Give the extent of all Plasmodium malariae-infected red blood cells.
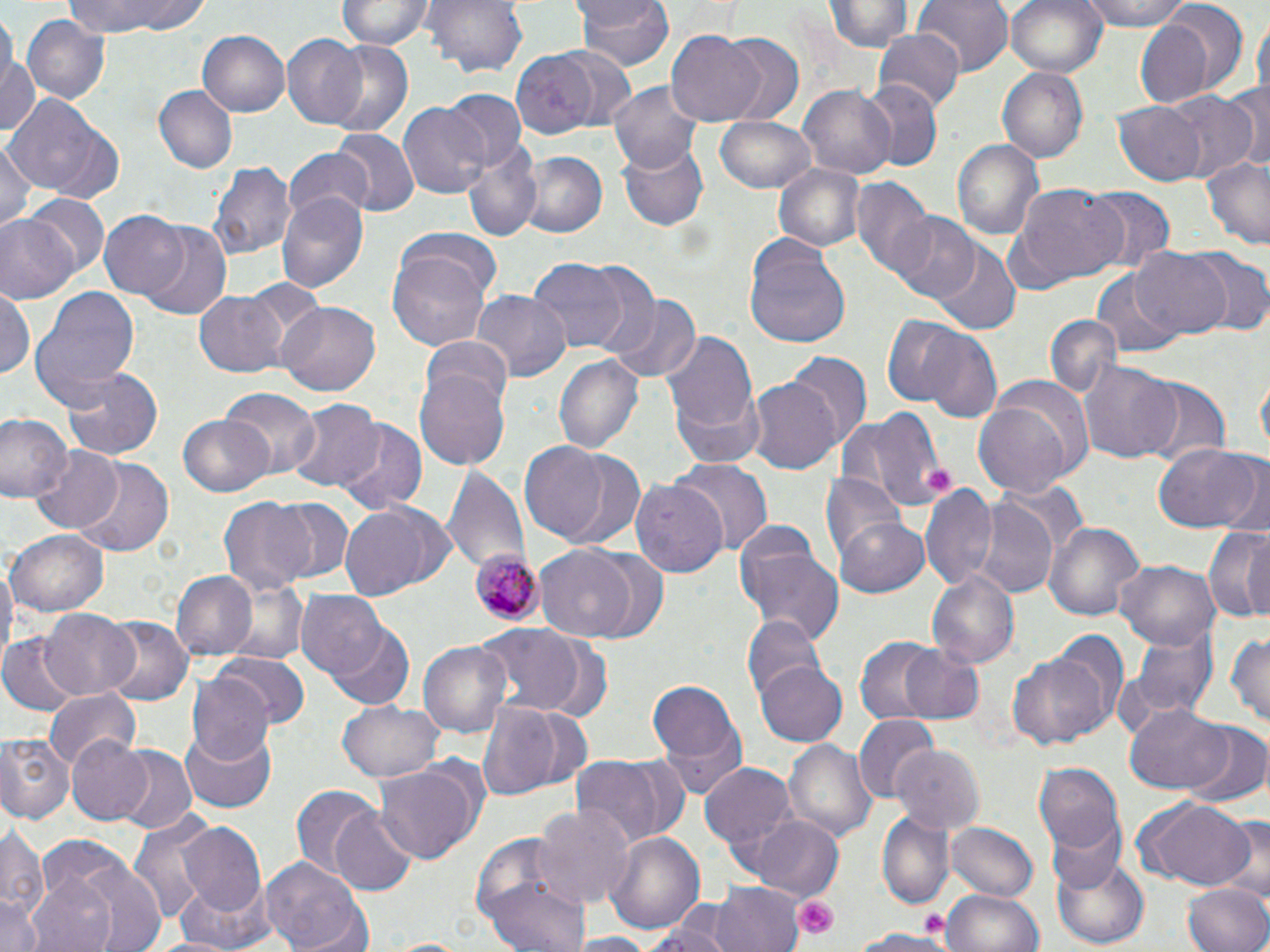

Approximate bounding boxes as named x1/y1/x2/y2 corners in pixels.
Plasmodium malariae-infected red blood cells: (x1=472, y1=549, x2=541, y2=626).

Platelet locations: (x1=795, y1=894, x2=840, y2=938), (x1=917, y1=909, x2=950, y2=945). Uninfected red blood cell locations: (x1=62, y1=0, x2=211, y2=38), (x1=424, y1=0, x2=529, y2=78), (x1=574, y1=0, x2=675, y2=74), (x1=826, y1=0, x2=909, y2=53), (x1=914, y1=0, x2=1013, y2=74), (x1=1006, y1=0, x2=1107, y2=80), (x1=1075, y1=0, x2=1200, y2=30), (x1=335, y1=1, x2=434, y2=52), (x1=4, y1=10, x2=19, y2=95), (x1=1134, y1=13, x2=1228, y2=106), (x1=1253, y1=14, x2=1269, y2=102), (x1=23, y1=15, x2=109, y2=103), (x1=197, y1=30, x2=290, y2=118), (x1=874, y1=30, x2=965, y2=114), (x1=719, y1=31, x2=804, y2=121), (x1=665, y1=32, x2=768, y2=122), (x1=280, y1=34, x2=369, y2=128), (x1=322, y1=41, x2=414, y2=138), (x1=0, y1=43, x2=40, y2=144), (x1=548, y1=43, x2=640, y2=133), (x1=509, y1=51, x2=614, y2=139), (x1=997, y1=67, x2=1089, y2=163), (x1=858, y1=79, x2=941, y2=170), (x1=607, y1=80, x2=707, y2=174), (x1=1226, y1=82, x2=1270, y2=171), (x1=155, y1=87, x2=237, y2=173), (x1=799, y1=87, x2=894, y2=178), (x1=441, y1=91, x2=527, y2=171), (x1=4, y1=92, x2=115, y2=199), (x1=1164, y1=92, x2=1259, y2=183), (x1=397, y1=101, x2=489, y2=200), (x1=1112, y1=103, x2=1205, y2=184), (x1=713, y1=115, x2=816, y2=194), (x1=331, y1=128, x2=419, y2=217), (x1=953, y1=138, x2=1045, y2=244), (x1=0, y1=139, x2=38, y2=234), (x1=616, y1=139, x2=707, y2=231), (x1=462, y1=142, x2=541, y2=240), (x1=282, y1=148, x2=374, y2=224), (x1=521, y1=151, x2=607, y2=239), (x1=1201, y1=156, x2=1270, y2=248), (x1=209, y1=160, x2=295, y2=260), (x1=774, y1=163, x2=865, y2=252), (x1=853, y1=180, x2=938, y2=281), (x1=1016, y1=185, x2=1130, y2=286), (x1=1085, y1=189, x2=1175, y2=270), (x1=277, y1=190, x2=369, y2=292), (x1=25, y1=194, x2=110, y2=278), (x1=101, y1=212, x2=192, y2=300), (x1=888, y1=212, x2=981, y2=304), (x1=0, y1=215, x2=77, y2=305), (x1=138, y1=224, x2=230, y2=319), (x1=399, y1=230, x2=502, y2=303), (x1=741, y1=239, x2=852, y2=352), (x1=931, y1=245, x2=1021, y2=333), (x1=1133, y1=247, x2=1233, y2=339), (x1=388, y1=250, x2=489, y2=349), (x1=1186, y1=251, x2=1270, y2=337), (x1=528, y1=257, x2=628, y2=355), (x1=581, y1=266, x2=663, y2=359), (x1=1090, y1=268, x2=1184, y2=359), (x1=31, y1=287, x2=141, y2=408), (x1=0, y1=289, x2=35, y2=381), (x1=473, y1=291, x2=569, y2=381), (x1=193, y1=293, x2=288, y2=375), (x1=605, y1=296, x2=699, y2=384), (x1=277, y1=302, x2=380, y2=396), (x1=1043, y1=315, x2=1123, y2=401), (x1=879, y1=316, x2=976, y2=407), (x1=915, y1=329, x2=1003, y2=425), (x1=662, y1=330, x2=759, y2=446), (x1=421, y1=336, x2=515, y2=420), (x1=787, y1=351, x2=871, y2=447), (x1=553, y1=352, x2=643, y2=456), (x1=1079, y1=360, x2=1178, y2=465), (x1=62, y1=366, x2=163, y2=461), (x1=417, y1=368, x2=510, y2=471), (x1=1257, y1=374, x2=1269, y2=459), (x1=747, y1=378, x2=845, y2=472), (x1=1137, y1=378, x2=1231, y2=469), (x1=672, y1=388, x2=768, y2=468), (x1=221, y1=390, x2=320, y2=477), (x1=974, y1=393, x2=1082, y2=494), (x1=287, y1=399, x2=383, y2=493), (x1=846, y1=411, x2=948, y2=511), (x1=0, y1=412, x2=69, y2=504), (x1=177, y1=415, x2=276, y2=498), (x1=338, y1=420, x2=426, y2=513), (x1=518, y1=441, x2=612, y2=542), (x1=1153, y1=443, x2=1263, y2=534), (x1=29, y1=446, x2=122, y2=534), (x1=547, y1=446, x2=650, y2=551), (x1=71, y1=457, x2=176, y2=556), (x1=1212, y1=457, x2=1269, y2=539), (x1=673, y1=458, x2=770, y2=556), (x1=442, y1=466, x2=531, y2=578), (x1=822, y1=472, x2=907, y2=562), (x1=631, y1=476, x2=730, y2=578), (x1=920, y1=484, x2=999, y2=592), (x1=218, y1=496, x2=315, y2=599), (x1=268, y1=496, x2=354, y2=584), (x1=971, y1=497, x2=1060, y2=597), (x1=342, y1=503, x2=452, y2=597), (x1=834, y1=514, x2=931, y2=596), (x1=1045, y1=521, x2=1145, y2=622), (x1=1203, y1=527, x2=1270, y2=625), (x1=7, y1=528, x2=109, y2=615), (x1=736, y1=538, x2=844, y2=646), (x1=537, y1=546, x2=638, y2=640), (x1=582, y1=550, x2=672, y2=644), (x1=0, y1=556, x2=16, y2=670), (x1=1115, y1=560, x2=1221, y2=649), (x1=170, y1=569, x2=258, y2=661), (x1=928, y1=571, x2=1019, y2=668), (x1=220, y1=579, x2=309, y2=665), (x1=296, y1=589, x2=388, y2=679), (x1=40, y1=608, x2=140, y2=700), (x1=743, y1=616, x2=826, y2=705), (x1=100, y1=617, x2=190, y2=708), (x1=327, y1=622, x2=416, y2=711), (x1=473, y1=623, x2=589, y2=713), (x1=1132, y1=627, x2=1219, y2=719), (x1=1227, y1=630, x2=1270, y2=731), (x1=1039, y1=631, x2=1129, y2=738), (x1=854, y1=635, x2=943, y2=726), (x1=0, y1=636, x2=81, y2=718), (x1=419, y1=640, x2=513, y2=741), (x1=898, y1=645, x2=988, y2=726), (x1=1008, y1=651, x2=1109, y2=751), (x1=216, y1=654, x2=308, y2=731), (x1=756, y1=660, x2=848, y2=747), (x1=187, y1=673, x2=274, y2=768), (x1=645, y1=674, x2=745, y2=790), (x1=44, y1=688, x2=140, y2=767), (x1=337, y1=700, x2=442, y2=783), (x1=477, y1=701, x2=560, y2=803), (x1=1122, y1=703, x2=1232, y2=794), (x1=519, y1=707, x2=592, y2=794), (x1=853, y1=716, x2=940, y2=802), (x1=179, y1=725, x2=278, y2=813), (x1=1184, y1=725, x2=1270, y2=809), (x1=0, y1=734, x2=73, y2=823), (x1=67, y1=734, x2=155, y2=826), (x1=786, y1=739, x2=877, y2=841), (x1=111, y1=746, x2=196, y2=835), (x1=894, y1=746, x2=984, y2=835), (x1=569, y1=751, x2=686, y2=847), (x1=702, y1=761, x2=799, y2=868), (x1=1034, y1=762, x2=1124, y2=856), (x1=376, y1=765, x2=479, y2=865), (x1=293, y1=787, x2=383, y2=880), (x1=1132, y1=798, x2=1257, y2=889), (x1=532, y1=801, x2=635, y2=910), (x1=328, y1=806, x2=420, y2=897), (x1=128, y1=807, x2=220, y2=927), (x1=877, y1=811, x2=954, y2=907), (x1=1043, y1=814, x2=1127, y2=894), (x1=751, y1=815, x2=842, y2=898), (x1=1223, y1=817, x2=1269, y2=901), (x1=177, y1=821, x2=271, y2=920), (x1=948, y1=823, x2=1039, y2=902), (x1=0, y1=824, x2=46, y2=928), (x1=470, y1=830, x2=579, y2=938), (x1=605, y1=831, x2=703, y2=937), (x1=1052, y1=852, x2=1150, y2=948), (x1=69, y1=857, x2=170, y2=952), (x1=258, y1=858, x2=370, y2=952), (x1=22, y1=867, x2=127, y2=952), (x1=484, y1=873, x2=589, y2=952), (x1=710, y1=881, x2=804, y2=952), (x1=1183, y1=883, x2=1270, y2=952), (x1=943, y1=888, x2=1043, y2=952), (x1=0, y1=894, x2=46, y2=952), (x1=652, y1=905, x2=738, y2=952), (x1=847, y1=926, x2=959, y2=951), (x1=562, y1=935, x2=663, y2=952), (x1=382, y1=938, x2=474, y2=952). Slide-level diagnosis: Plasmodium malariae. Single field of view. Thin blood smear. May-Grünwald-Giemsa stain. Image is 1270×952 pixels. 1000x magnification. Light microscopy.